Give the extent of all Plasmodium vivax-infected red blood cells.
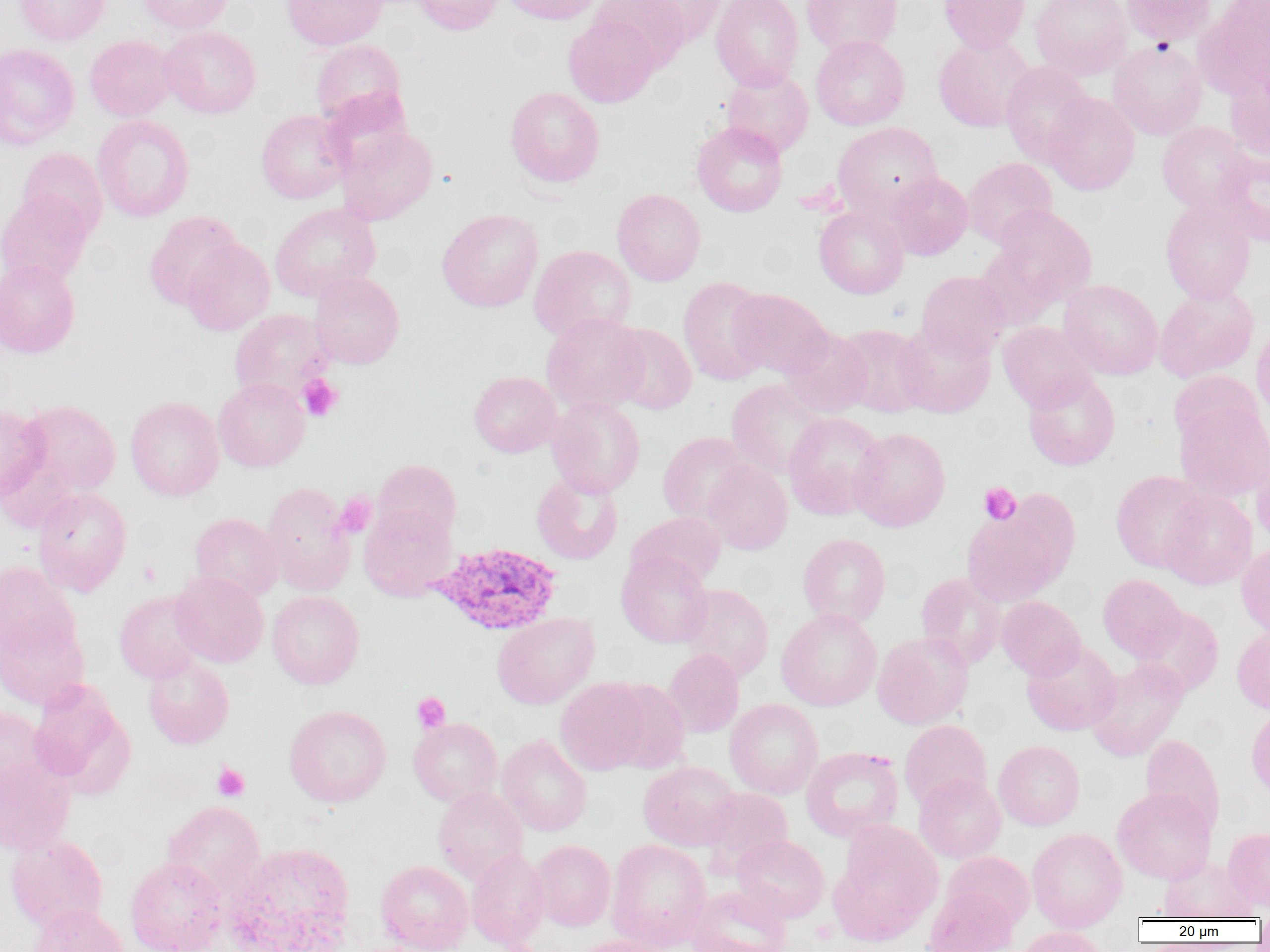
Approximate bounding boxes as [x1, y1, x2, y2] in pixels.
Plasmodium vivax-infected red blood cells: [426, 542, 563, 636].

slide-level diagnosis = Plasmodium vivax
modality = optical microscopy
image size = 1270×952 pixels
platelet locations = approximate bounding boxes as [x1, y1, x2, y2] in pixels: [298, 374, 343, 422], [979, 482, 1021, 525], [336, 493, 376, 538], [412, 693, 450, 732], [212, 763, 249, 801]
preparation = thin blood smear
uninfected red blood cell locations = approximate bounding boxes as [x1, y1, x2, y2] in pixels: [14, 0, 110, 45], [137, 0, 233, 33], [282, 0, 388, 50], [411, 0, 503, 34], [501, 0, 603, 24], [592, 0, 691, 72], [631, 0, 728, 46], [711, 0, 803, 91], [801, 0, 903, 56], [938, 0, 1031, 52], [1031, 0, 1132, 80], [1121, 0, 1218, 45], [1202, 0, 1270, 95], [564, 15, 660, 107], [159, 26, 260, 118], [810, 35, 909, 130], [934, 35, 1035, 132], [84, 36, 176, 121], [310, 39, 406, 128], [1109, 40, 1207, 139], [0, 43, 79, 149], [1000, 61, 1096, 165], [720, 67, 813, 159], [1225, 69, 1270, 164], [505, 87, 604, 187], [1042, 92, 1139, 195], [256, 110, 351, 203], [92, 115, 194, 221], [1157, 121, 1254, 214], [692, 122, 788, 216], [833, 122, 942, 217], [336, 125, 437, 225], [17, 148, 108, 240], [1215, 151, 1270, 246], [962, 157, 1058, 248], [887, 172, 973, 260], [612, 189, 705, 286], [0, 191, 92, 288], [1161, 199, 1255, 303], [270, 203, 380, 302], [992, 205, 1096, 305], [814, 206, 909, 299], [437, 209, 543, 312], [144, 211, 243, 309], [181, 238, 275, 335], [975, 244, 1063, 331], [529, 245, 636, 342], [0, 260, 80, 358], [916, 271, 1010, 359], [309, 272, 404, 368], [678, 276, 773, 386], [1059, 279, 1163, 380], [1154, 285, 1258, 382], [728, 288, 831, 378], [230, 309, 333, 401], [541, 313, 649, 414], [998, 321, 1097, 412], [895, 322, 996, 418], [608, 323, 697, 414], [835, 324, 932, 417], [780, 326, 873, 418], [1252, 326, 1270, 419], [1168, 371, 1264, 451], [469, 372, 561, 457], [1023, 373, 1120, 470], [214, 378, 310, 471], [726, 379, 828, 479], [125, 396, 224, 500], [547, 396, 644, 497], [17, 400, 120, 496], [1175, 401, 1270, 502], [0, 406, 49, 501], [783, 412, 886, 519], [849, 427, 950, 531], [658, 432, 752, 524], [1, 451, 83, 532], [1251, 454, 1270, 548], [372, 459, 461, 543], [703, 460, 792, 555], [1111, 470, 1209, 572], [531, 472, 623, 565], [261, 482, 357, 596], [32, 487, 131, 596], [1159, 489, 1257, 589], [359, 504, 457, 601], [961, 509, 1065, 606], [627, 512, 726, 590], [190, 513, 283, 602], [798, 534, 890, 628], [1236, 542, 1270, 636], [616, 552, 713, 648], [0, 562, 80, 661], [170, 571, 268, 667], [916, 573, 1006, 668], [1098, 575, 1185, 661], [679, 584, 774, 682], [114, 590, 208, 683], [267, 590, 364, 689], [996, 596, 1085, 680], [1134, 606, 1223, 697], [776, 608, 882, 711], [492, 612, 599, 708], [0, 616, 88, 710], [1232, 625, 1270, 713], [872, 632, 972, 729], [1021, 640, 1121, 735], [662, 649, 744, 737], [143, 655, 234, 748], [1086, 658, 1188, 761], [556, 678, 650, 775], [604, 679, 691, 774], [28, 680, 131, 794], [725, 699, 823, 799], [283, 704, 391, 807], [0, 706, 48, 800], [1246, 706, 1270, 798], [408, 718, 503, 807], [899, 720, 992, 810], [1141, 734, 1225, 834], [497, 735, 592, 836], [994, 740, 1084, 830], [801, 746, 903, 842], [0, 756, 75, 855], [638, 761, 740, 850], [914, 773, 1006, 863], [433, 787, 527, 883], [699, 787, 793, 875], [1113, 787, 1216, 883], [163, 801, 265, 898], [833, 820, 944, 940], [1223, 827, 1270, 911], [1027, 828, 1127, 931], [6, 834, 108, 932], [732, 834, 829, 922], [606, 839, 711, 951], [530, 840, 615, 931], [228, 842, 357, 952], [466, 848, 550, 949], [942, 851, 1034, 930], [1158, 856, 1256, 920], [125, 857, 227, 952], [376, 861, 473, 952], [686, 886, 792, 952], [923, 887, 1016, 952], [28, 903, 127, 952], [1014, 927, 1110, 952], [569, 936, 668, 952]
field of view = one of a larger specimen
magnification = 1000x